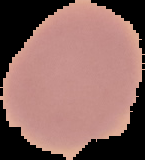
Summary:
  - Malaria status: uninfected
  - Preparation: thin blood film
  - Image type: cell region segmented out of the field of view; surrounding area masked to black
  - Image size: 145×160 pixels